Report the malaria status of this cell.
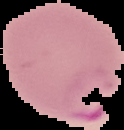

Parasitized.

image type = segmented cell region with the area outside set to black
preparation = thin blood smear
image size = 124×130 pixels